Assess this cell for malaria.
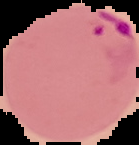

Parasitized.

image size = 139×145 pixels
image type = segmented cell region on a black background
preparation = thin blood smear